Describe the morphology of the erythrocytes.
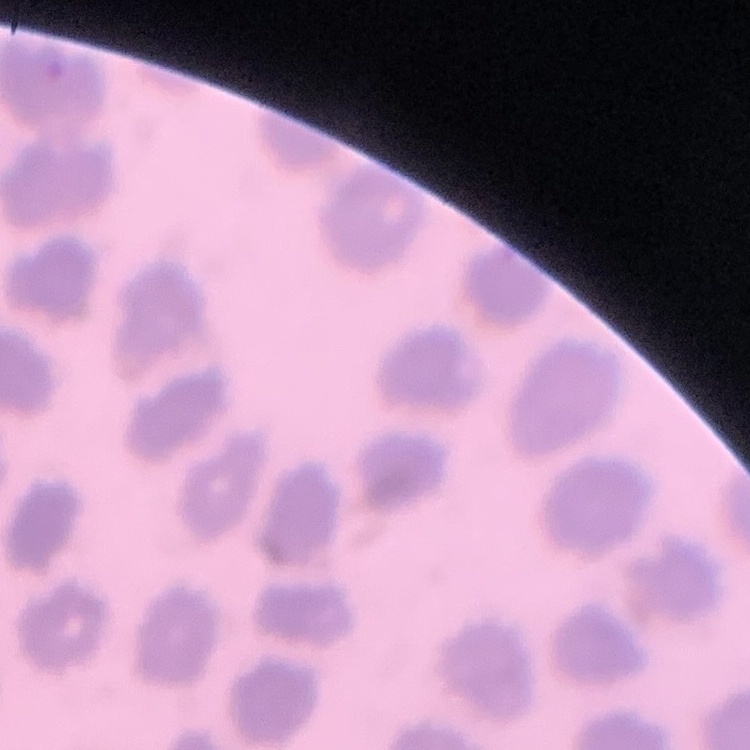

They show no rouleaux formation.

Summary:
  - Image type: one tile cut from a larger photomicrograph
  - Stain: Field's or Giemsa
  - Preparation: thin blood smear